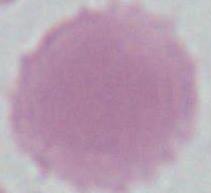
identification = erythrocyte
modality = photomicrograph
magnification = 1000x